Locate every Plasmodium parasite.
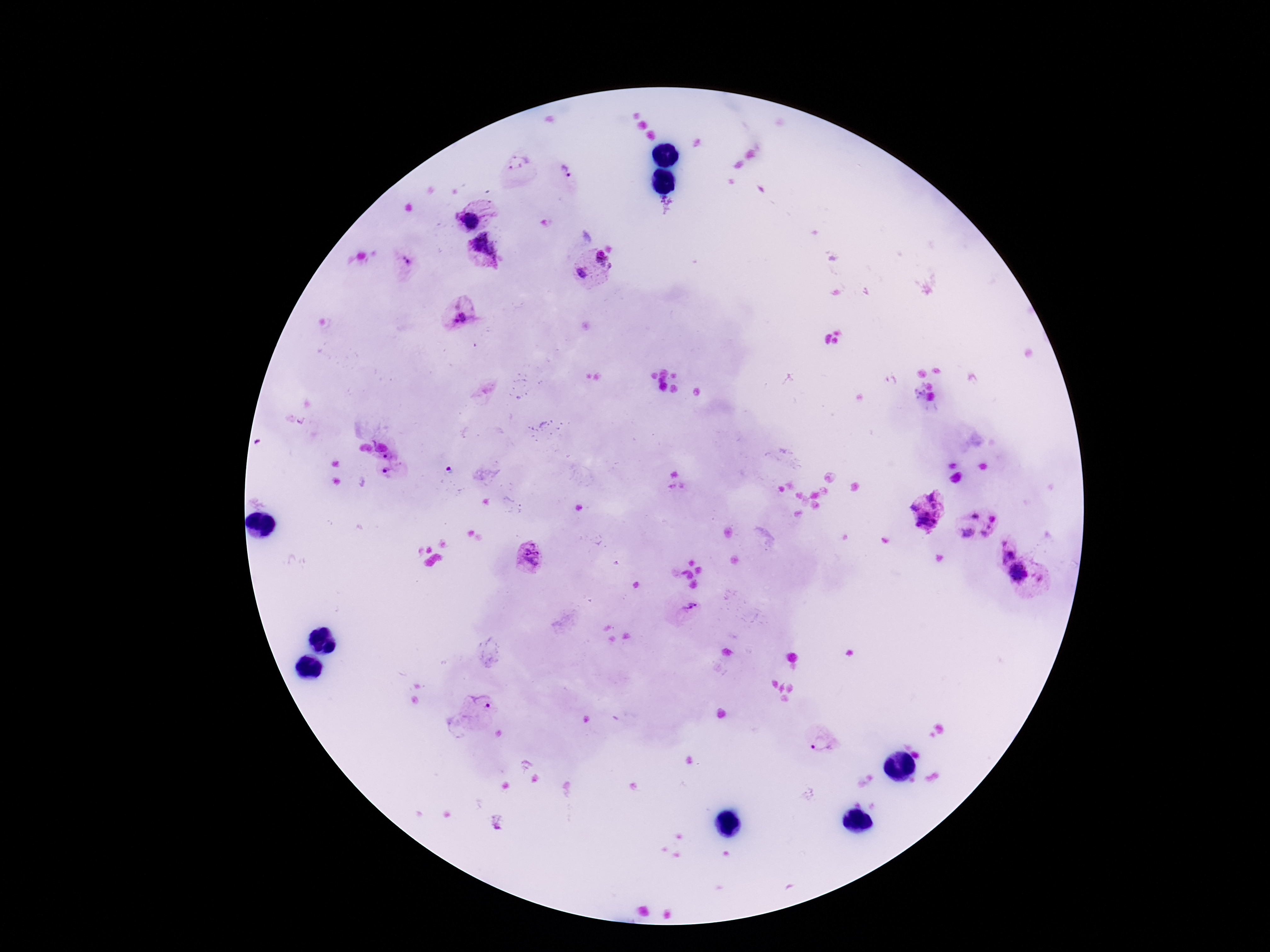
Approximate centers as [x, y] in pixels.
Plasmodium parasites: [518, 162], [564, 173], [475, 213], [484, 252], [601, 260], [405, 263], [581, 274], [463, 319], [389, 454], [390, 471], [449, 472], [926, 509], [977, 524], [1006, 548], [530, 556], [1018, 573], [688, 608], [480, 708], [822, 744].

image size = 1270×952 pixels
capture = smartphone camera through the microscope eyepiece
magnification = 100x
stain = Giemsa
preparation = thick blood film
patient malaria status = positive
field of view = one from this slide